Assess this cell for malaria.
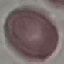
It is uninfected.

Automatically extracted cell patch, resized to 64 × 64 pixels. Thin blood smear. Giemsa-stained preparation. Photographed with a smartphone camera at the microscope eyepiece.